Outline each Plasmodium ovale-infected red blood cell.
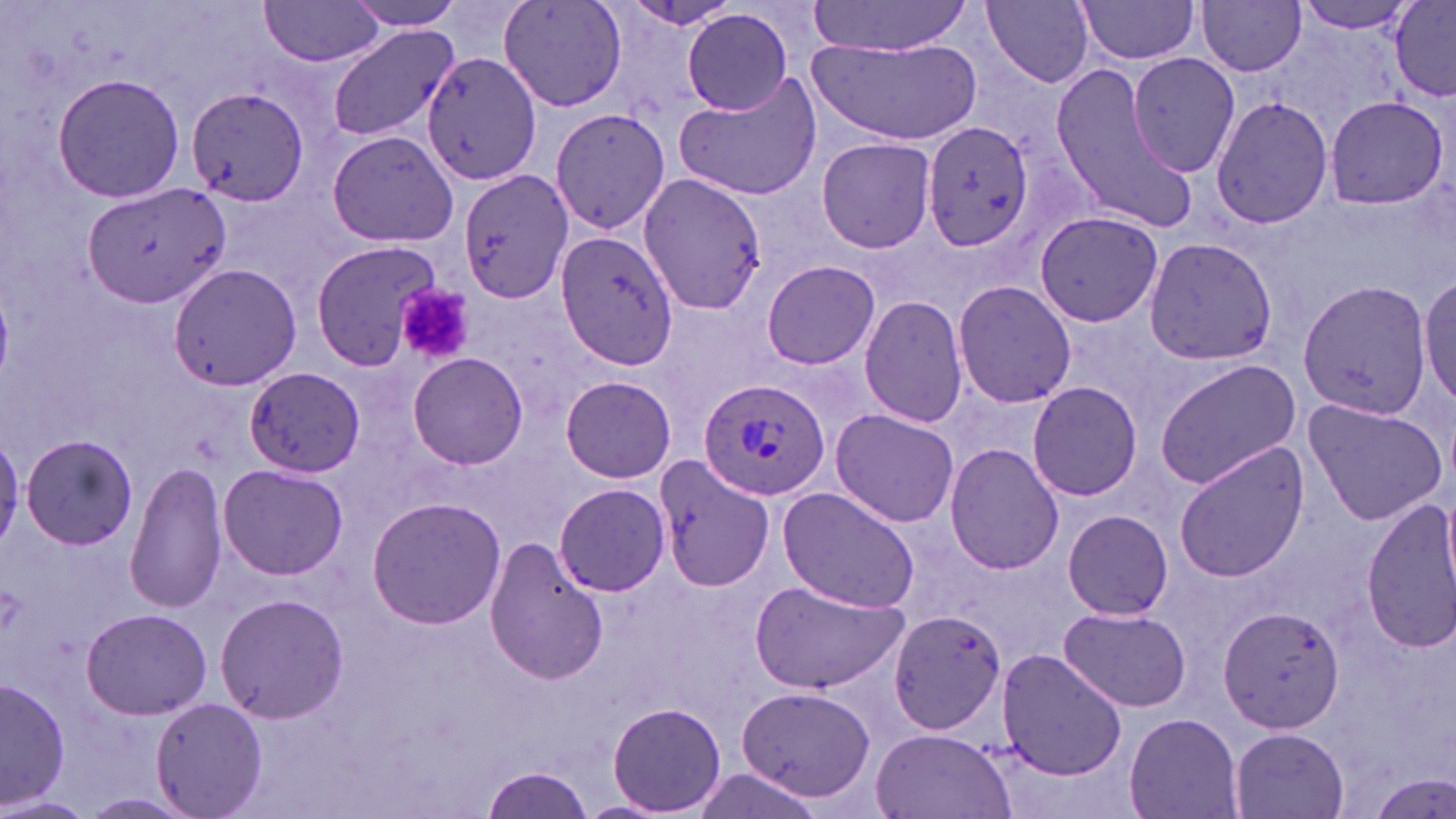

Approximate bounding boxes as [x1, y1, x2, y2] in pixels.
Plasmodium ovale-infected red blood cells: [698, 374, 832, 503].

Platelet locations: [397, 284, 473, 365]. Uninfected red blood cell locations: [498, 0, 627, 111], [1298, 0, 1423, 34], [1390, 0, 1456, 100], [257, 1, 387, 68], [343, 1, 468, 32], [624, 1, 741, 31], [807, 1, 973, 56], [983, 1, 1096, 88], [1197, 1, 1308, 76], [1075, 2, 1205, 68], [681, 8, 797, 115], [327, 25, 458, 143], [811, 37, 979, 144], [1126, 50, 1241, 178], [423, 52, 546, 190], [1047, 64, 1194, 226], [51, 73, 186, 205], [676, 75, 821, 201], [185, 87, 308, 208], [1210, 93, 1334, 231], [1322, 96, 1449, 209], [550, 105, 671, 237], [922, 120, 1035, 252], [326, 130, 457, 246], [816, 136, 937, 254], [459, 168, 574, 302], [639, 172, 769, 313], [84, 184, 229, 309], [1035, 210, 1165, 329], [557, 231, 680, 372], [1142, 238, 1278, 365], [309, 240, 441, 371], [762, 259, 881, 370], [168, 264, 302, 392], [1418, 273, 1455, 413], [951, 279, 1076, 409], [1296, 280, 1431, 419], [860, 294, 970, 428], [408, 352, 528, 469], [1154, 357, 1304, 489], [245, 366, 366, 475], [562, 375, 675, 484], [1026, 381, 1142, 501], [1301, 396, 1448, 525], [830, 409, 959, 527], [0, 426, 24, 556], [22, 433, 140, 550], [944, 443, 1065, 575], [1174, 443, 1311, 584], [655, 457, 773, 594], [126, 461, 228, 614], [219, 463, 347, 580], [554, 483, 670, 597], [776, 485, 921, 613], [368, 496, 506, 629], [1361, 497, 1456, 651], [1061, 510, 1173, 621], [485, 536, 608, 685], [750, 579, 908, 697], [215, 591, 347, 724], [1218, 603, 1346, 734], [1058, 607, 1192, 710], [82, 609, 213, 718], [885, 610, 1007, 734], [993, 647, 1128, 780], [1, 678, 70, 811], [736, 684, 877, 804], [149, 696, 267, 819], [611, 703, 726, 814], [1123, 712, 1245, 819], [1228, 727, 1352, 818], [869, 728, 1016, 819], [482, 768, 590, 817], [1368, 769, 1455, 818], [0, 794, 92, 819]. Slide-level diagnosis: Plasmodium ovale. Image is 1456×819 pixels. One field of a larger specimen. May-Grünwald-Giemsa stain. 1000x magnification. Thin blood smear. Optical microscopy.